Comment on the background quality.
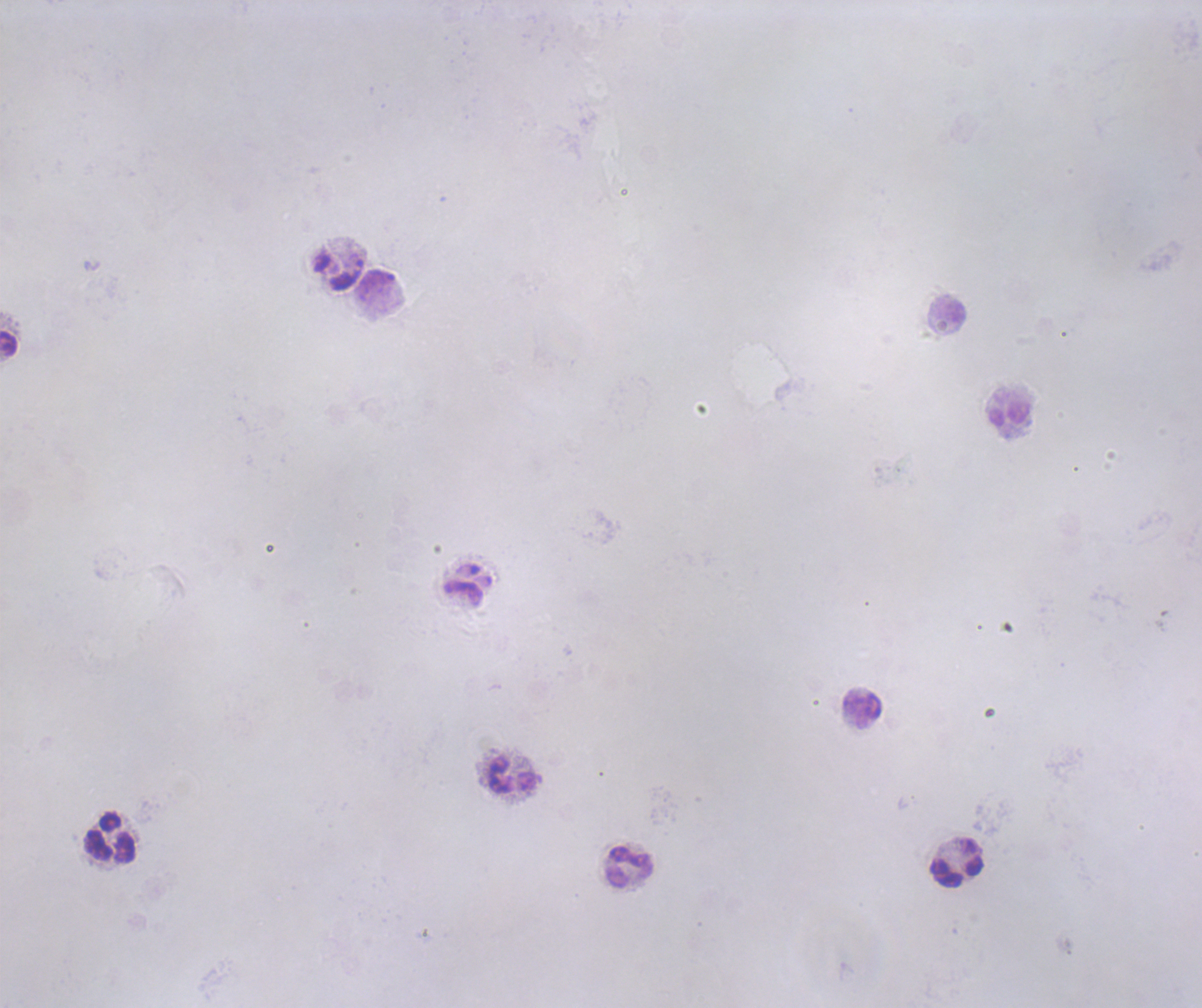

It is poor.

Approximate object centers, in pixels from the top-left corner.
Summary:
  - Leukocyte locations: (x=339, y=272), (x=376, y=285), (x=947, y=309), (x=9, y=344), (x=1010, y=415), (x=468, y=584), (x=863, y=709), (x=512, y=776), (x=109, y=838), (x=956, y=863), (x=629, y=867)
  - Coloration quality: bad
  - Image size: 1202×1008 pixels
  - Context: previously used in an actual diagnosis
  - Field of view: single
  - Preparation: thick blood smear
  - Stain: Romanowsky
  - Magnification: 100x
  - Result: no Plasmodium parasites detected